State the blood parasite species.
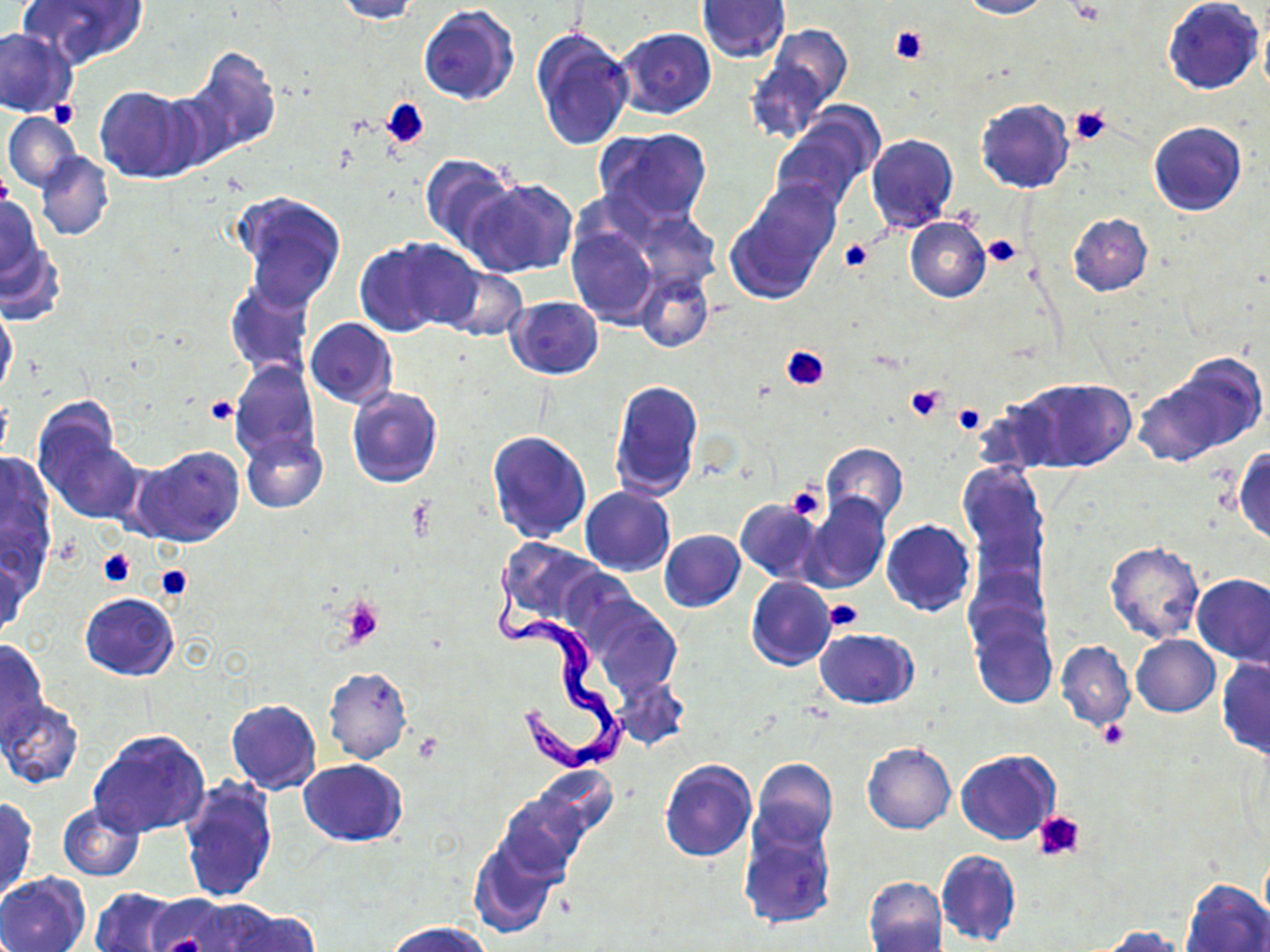

Trypanosoma brucei.

image size = 1270×952 pixels
stain = May-Grünwald-Giemsa
preparation = thin blood smear
uninfected red blood cell locations = approximate bounding boxes as (x1, y1, x2, y2) in pixels: (17, 0, 148, 71), (329, 0, 423, 22), (697, 0, 791, 63), (959, 0, 1052, 18), (1163, 0, 1264, 94), (704, 4, 836, 87), (418, 5, 519, 106), (1259, 18, 1270, 101), (759, 24, 852, 122), (530, 26, 633, 151), (0, 27, 77, 117), (613, 27, 716, 121), (183, 49, 280, 159), (97, 87, 200, 181), (976, 98, 1073, 193), (4, 111, 81, 191), (770, 117, 876, 216), (1148, 121, 1247, 215), (594, 127, 712, 230), (866, 133, 958, 233), (36, 151, 113, 241), (418, 152, 516, 250), (465, 178, 577, 278), (727, 188, 839, 301), (231, 191, 347, 309), (0, 195, 43, 282), (564, 195, 722, 338), (1068, 214, 1153, 295), (905, 216, 990, 302), (567, 225, 658, 328), (358, 238, 478, 336), (1, 239, 63, 325), (444, 267, 527, 342), (636, 270, 712, 353), (225, 281, 315, 380), (504, 296, 604, 379), (0, 302, 17, 398), (305, 317, 397, 407), (1134, 352, 1267, 465), (230, 360, 320, 467), (1014, 376, 1135, 473), (609, 378, 704, 501), (346, 388, 443, 488), (32, 400, 135, 523), (485, 429, 591, 543), (240, 433, 327, 513), (821, 443, 908, 526), (135, 445, 245, 547), (1233, 446, 1270, 546), (0, 456, 59, 591), (959, 462, 1048, 585), (581, 486, 676, 577), (801, 493, 891, 593), (735, 498, 821, 582), (881, 520, 976, 617), (659, 529, 746, 613), (495, 537, 606, 630), (1105, 542, 1204, 645), (1, 553, 28, 641), (1192, 574, 1270, 665), (747, 577, 836, 671), (80, 591, 180, 681), (586, 599, 681, 697), (969, 612, 1057, 711), (815, 629, 919, 709), (1131, 635, 1220, 717), (0, 637, 49, 747), (1057, 641, 1134, 729), (1217, 657, 1270, 758), (322, 666, 412, 764), (612, 675, 688, 751), (521, 684, 618, 768), (2, 698, 84, 790), (226, 698, 321, 795), (88, 729, 210, 838), (862, 742, 957, 835), (955, 750, 1060, 845), (299, 758, 407, 847), (751, 758, 838, 849), (659, 760, 757, 862), (531, 766, 618, 842), (180, 776, 278, 905), (496, 794, 587, 881), (1, 797, 37, 901), (57, 802, 144, 880), (737, 815, 838, 930), (469, 839, 559, 937), (935, 848, 1021, 947), (0, 872, 90, 952), (864, 875, 948, 952), (1182, 877, 1270, 952), (90, 887, 185, 951), (148, 894, 253, 951), (215, 905, 320, 952), (387, 921, 491, 952), (1095, 925, 1189, 951)
modality = light microscopy
field of view = single
Trypanosoma brucei locations = approximate bounding boxes as (x1, y1, x2, y2) in pixels: (489, 563, 633, 772)
magnification = 1000x
platelet locations = approximate bounding boxes as (x1, y1, x2, y2) in pixels: (889, 25, 929, 66), (50, 99, 78, 128), (382, 99, 429, 149), (1069, 105, 1112, 146), (0, 168, 12, 211), (982, 234, 1023, 268), (838, 237, 873, 273), (779, 345, 829, 391), (905, 383, 948, 423), (204, 395, 239, 424), (953, 403, 987, 433), (785, 482, 825, 523), (98, 548, 135, 585), (151, 565, 193, 603), (337, 596, 384, 648), (823, 599, 865, 631), (1099, 720, 1130, 749), (1034, 809, 1086, 862)